Report the malaria status of this cell.
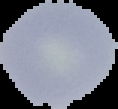
It is uninfected.

Segmented cell region on a black background. Image is 118×109 pixels. From a thin blood smear.